Comment on the morphology of the erythrocytes.
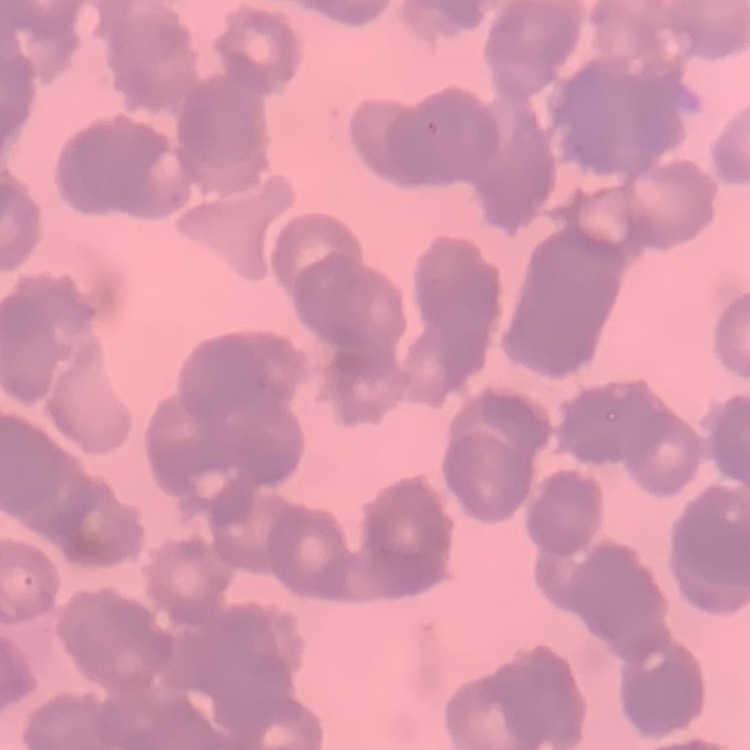
Rouleaux formation.

stain = Field's or Giemsa
image type = one tile cut from a larger photomicrograph
preparation = thin peripheral smear